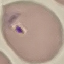

Summary:
  - Result: malaria parasites detected
  - Image type: cell patch, automatically extracted from a larger field of view and resized to 64 × 64 pixels
  - Stain: Giemsa
  - Capture: smartphone camera at the microscope eyepiece
  - Preparation: thin blood smear